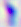

Micrograph. Toxoplasma gondii is shown. 400x magnification.